Report the malaria status of this cell.
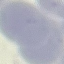

Uninfected.

Summary:
  - Preparation: thin blood smear
  - Stain: Giemsa
  - Capture: smartphone through the microscope eyepiece
  - Image type: cell patch, automatically extracted from a larger field of view and resized to 64 × 64 pixels